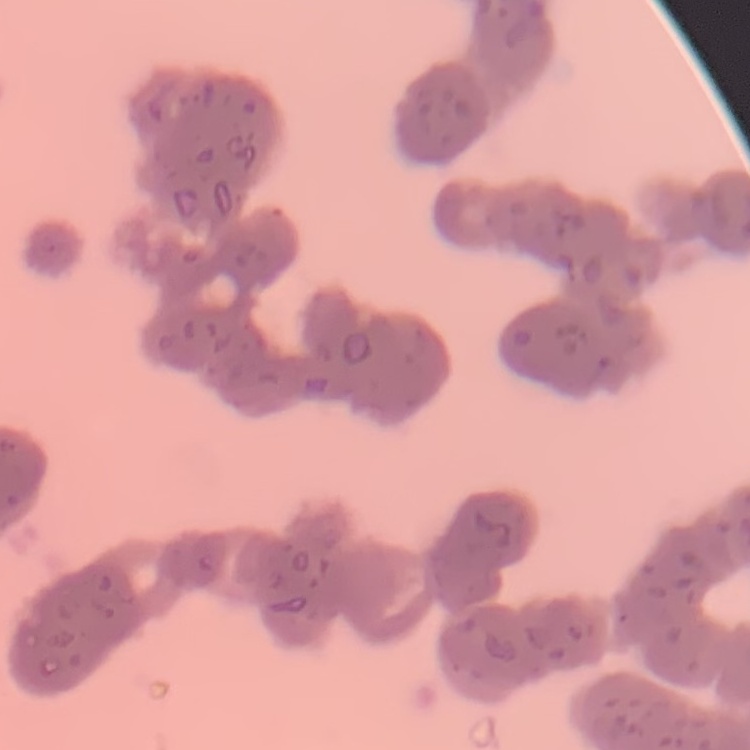
Summary:
  - Red blood cell morphology: rouleaux formation
  - Image type: square crop of a larger photomicrograph
  - Stain: Field's or Giemsa
  - Preparation: thin peripheral smear